Give the position of every Plasmodium parasite and every leukocyte.
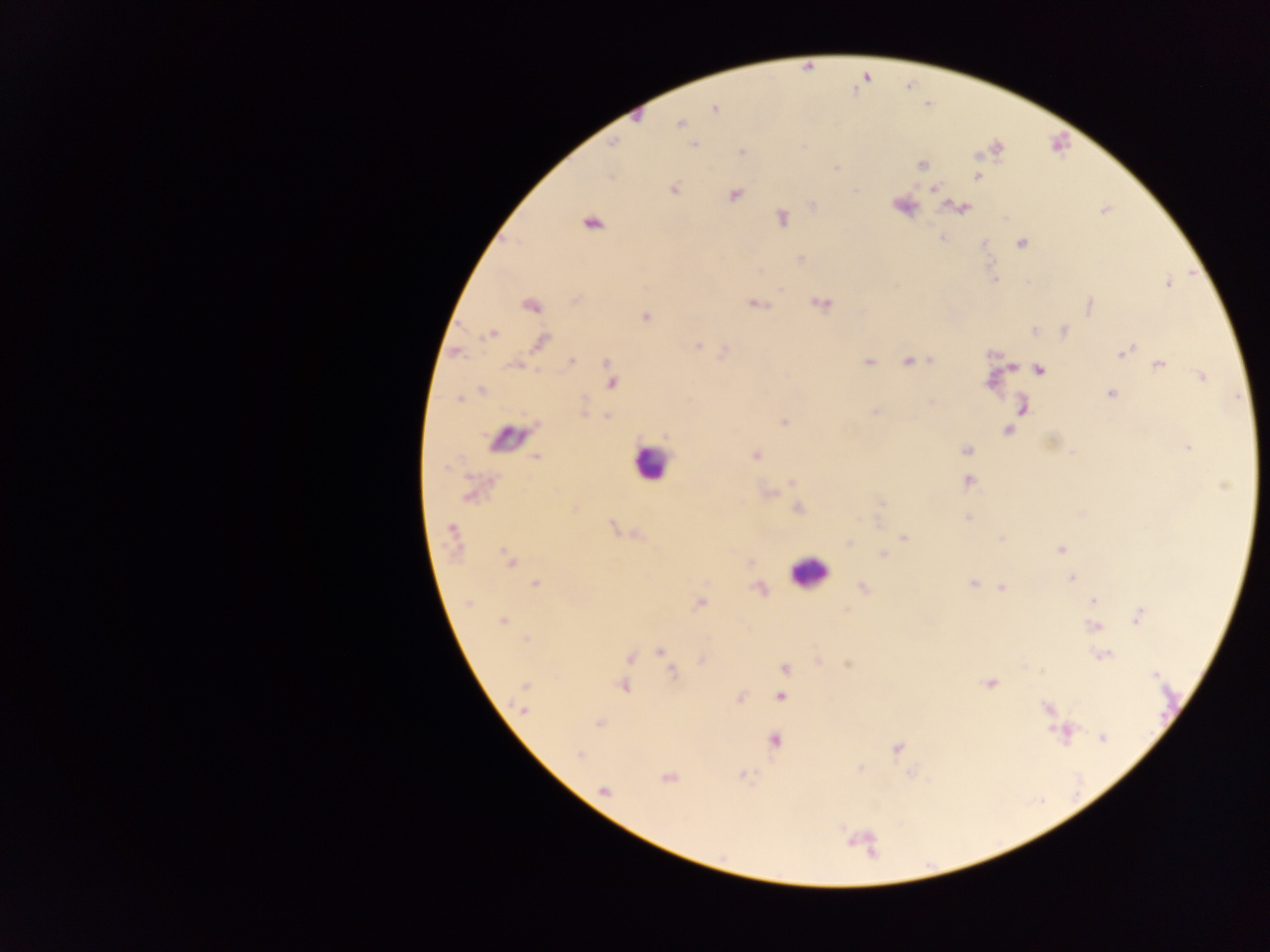
Approximate centers as {x, y} in pixels.
Plasmodium parasites: {678, 123}, {615, 141}, {693, 143}, {996, 147}, {740, 152}, {922, 164}, {836, 168}, {977, 177}, {933, 187}, {673, 188}, {735, 195}, {814, 204}, {900, 206}, {960, 208}, {782, 217}, {591, 223}, {942, 237}, {1022, 243}, {800, 258}, {1169, 284}, {576, 299}, {819, 303}, {754, 304}, {528, 306}, {1088, 306}, {645, 315}, {1035, 331}, {1065, 331}, {493, 333}, {488, 335}, {539, 341}, {697, 345}, {1132, 348}, {722, 350}, {456, 352}, {991, 353}, {1122, 353}, {572, 360}, {868, 360}, {909, 361}, {607, 362}, {1161, 363}, {516, 364}, {1009, 365}, {1038, 370}, {1200, 376}, {990, 382}, {612, 384}, {482, 389}, {1110, 392}, {458, 399}, {584, 399}, {931, 402}, {1022, 404}, {877, 411}, {584, 413}, {607, 415}, {784, 422}, {535, 425}, {1007, 430}, {1048, 443}, {1187, 448}, {968, 450}, {754, 455}, {1074, 455}, {536, 456}, {447, 468}, {969, 480}, {791, 481}, {768, 492}, {881, 502}, {798, 508}, {967, 518}, {878, 521}, {614, 528}, {452, 531}, {904, 535}, {1002, 537}, {848, 543}, {1058, 549}, {883, 553}, {507, 556}, {750, 561}, {1071, 579}, {536, 582}, {972, 582}, {862, 587}, {758, 589}, {1002, 589}, {1093, 600}, {469, 602}, {701, 602}, {1140, 614}, {1137, 620}, {503, 621}, {1095, 625}, {657, 651}, {1103, 654}, {628, 657}, {817, 658}, {701, 661}, {847, 662}, {784, 667}, {672, 673}, {1155, 676}, {991, 683}, {623, 686}, {780, 696}, {741, 697}, {524, 709}, {597, 725}, {1102, 738}, {774, 740}, {897, 749}, {579, 755}, {861, 767}, {913, 773}, {741, 774}, {670, 779}.
Leukocytes: {507, 440}, {647, 470}, {811, 578}.

image size = 1270×952 pixels
preparation = thick blood film
field of view = single
capture = mobile-phone photograph through a microscope
country = Ghana